Classify this cell by malaria status.
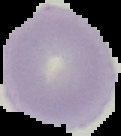
It is uninfected.

image size = 121×136 pixels
image type = cell region segmented out of the field of view; surrounding area masked to black
preparation = thin blood smear